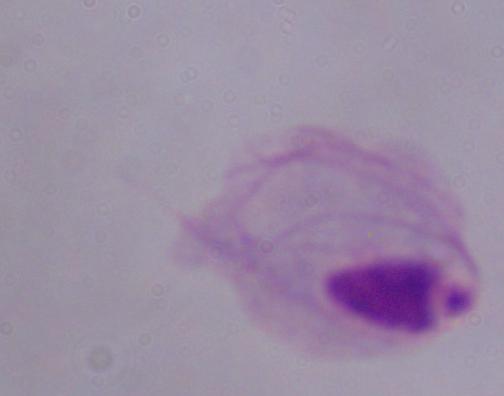
Summary:
  - Magnification: 1000x
  - Identification: trichomonad
  - Modality: photomicrograph